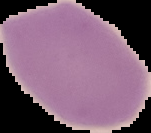
{
  "image_type": "segmented cell region with the area outside set to black",
  "malaria_status": "uninfected",
  "image_size": "151×133 pixels",
  "preparation": "thin blood film"
}